Assess this cell for malaria.
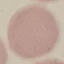
It is uninfected.

stain = Giemsa
preparation = thin blood smear
capture = smartphone through the microscope eyepiece
image type = automatically extracted cell patch, resized to 64 × 64 pixels